Report the malaria status of this cell.
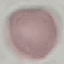
It is uninfected.

{
  "preparation": "thin blood film",
  "image_type": "cell patch, automatically extracted from a larger field of view and resized to 64 × 64 pixels",
  "capture": "smartphone through the microscope eyepiece",
  "stain": "Giemsa"
}